Assess this cell for malaria.
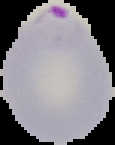

Parasitized.

Segmented cell region on a black background. From a thin blood smear. Image is 115×145 pixels.